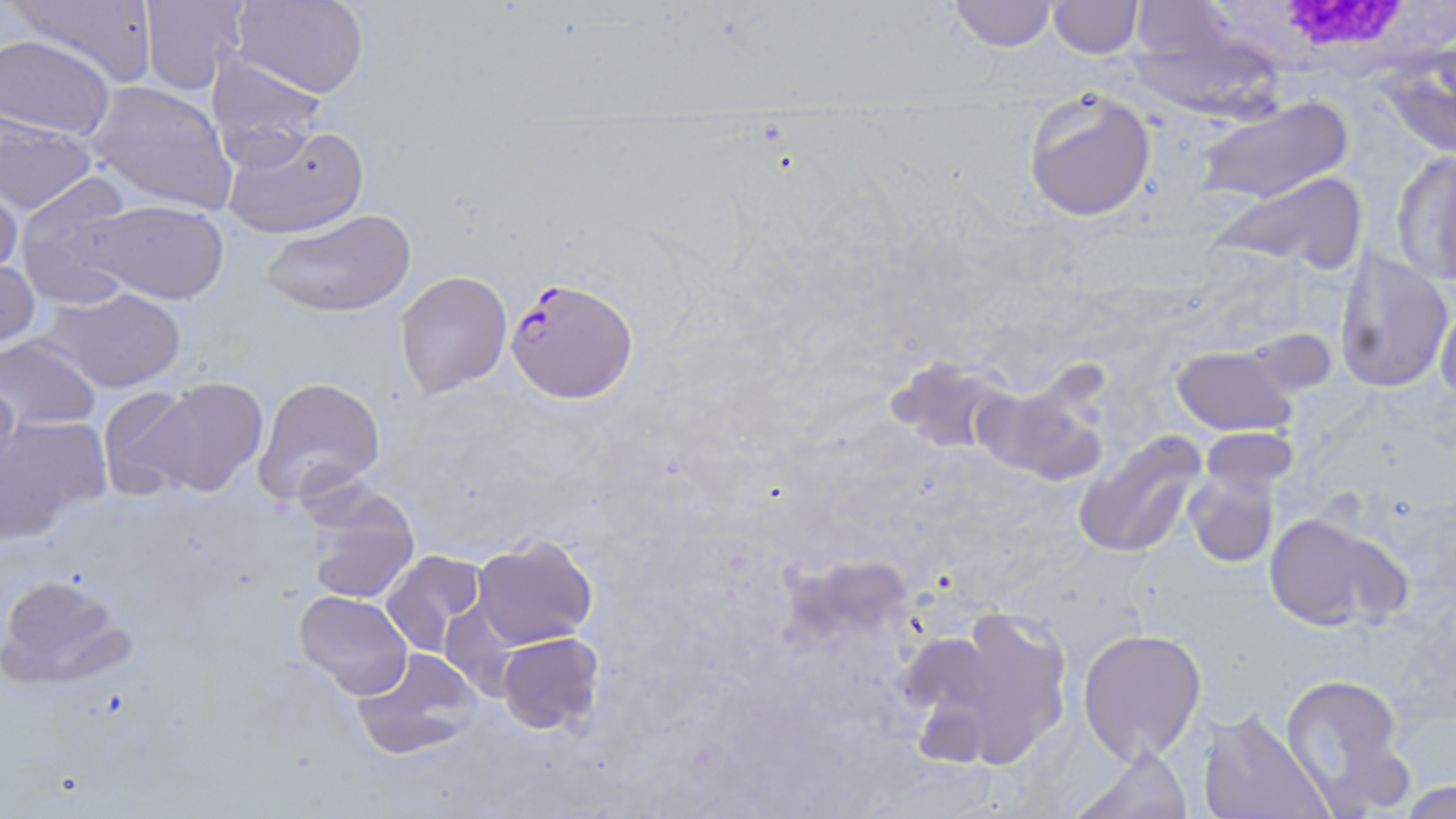
slide-level diagnosis = Plasmodium falciparum
white blood cell locations = approximate bounding boxes as [x1, y1, x2, y2] in pixels: [1201, 2, 1455, 85]
Plasmodium falciparum-infected red blood cell locations = approximate bounding boxes as [x1, y1, x2, y2] in pixels: [505, 276, 640, 403]
uninfected red blood cell locations = approximate bounding boxes as [x1, y1, x2, y2] in pixels: [12, 0, 161, 88], [232, 0, 369, 98], [944, 0, 1058, 51], [1047, 0, 1142, 56], [139, 1, 249, 92], [1124, 10, 1293, 120], [0, 35, 114, 142], [1371, 46, 1456, 159], [205, 54, 327, 172], [87, 80, 240, 214], [1021, 88, 1156, 222], [1193, 96, 1351, 206], [0, 112, 99, 214], [219, 122, 369, 240], [1390, 149, 1456, 284], [1205, 173, 1368, 274], [14, 174, 141, 309], [1, 177, 25, 282], [84, 199, 230, 304], [263, 208, 417, 317], [1334, 246, 1453, 395], [0, 257, 40, 351], [394, 272, 512, 398], [45, 286, 188, 394], [1434, 299, 1456, 405], [0, 337, 103, 430], [1169, 343, 1299, 437], [884, 353, 1018, 456], [0, 370, 20, 490], [252, 375, 387, 507], [974, 376, 1110, 487], [140, 377, 269, 498], [99, 383, 215, 500], [0, 415, 109, 540], [1074, 427, 1210, 560], [1198, 428, 1301, 495], [1181, 466, 1279, 570], [299, 486, 419, 607], [1261, 512, 1408, 632], [471, 535, 597, 648], [381, 548, 489, 657], [0, 572, 135, 690], [294, 590, 413, 699], [900, 605, 1077, 771], [1076, 627, 1207, 765], [498, 631, 603, 733], [348, 647, 483, 760], [1279, 673, 1414, 812], [1194, 707, 1333, 819], [1069, 743, 1191, 819], [1401, 780, 1453, 818]
image size = 1456×819 pixels
magnification = 1000x
stain = May-Grünwald-Giemsa
modality = light microscopy
preparation = thin blood smear
field of view = one of a larger specimen